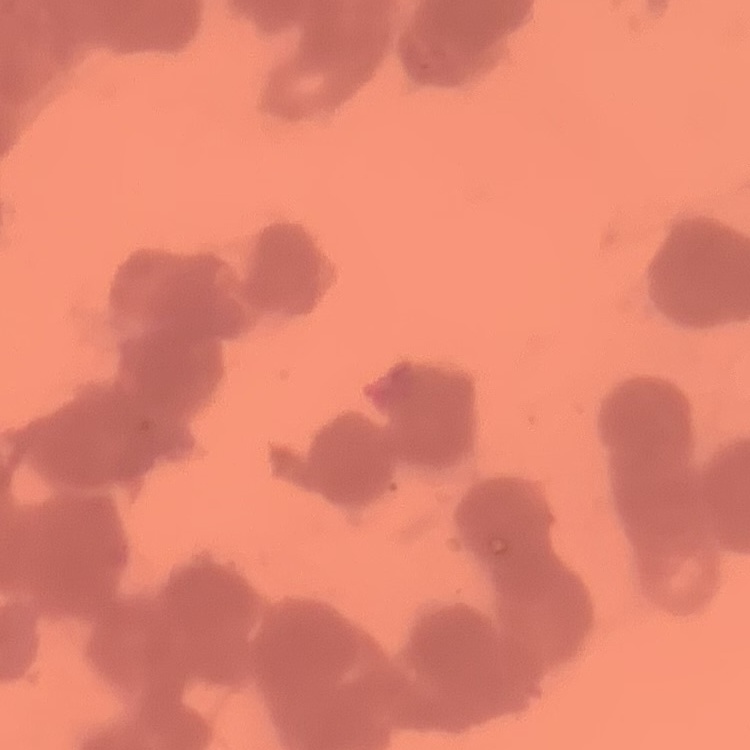 The erythrocytes show rouleaux formation. One tile cut from a larger photomicrograph. Field's or Giemsa stain. Thin blood film.